Report the malaria status of this cell.
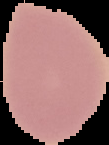

Uninfected.

image type = segmented cell region on a black background
image size = 109×145 pixels
preparation = thin blood smear